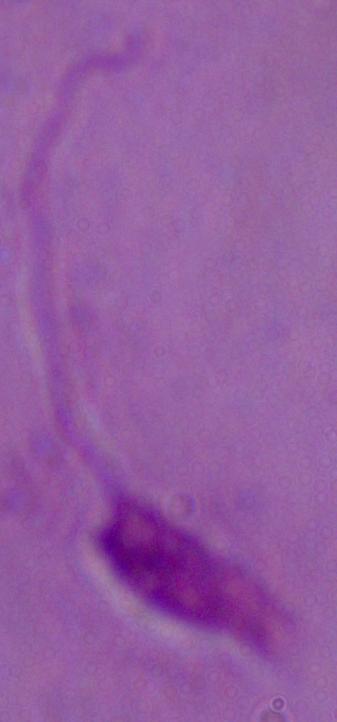

Summary:
  - Identification: Leishmania
  - Modality: photomicrograph
  - Magnification: 1000x